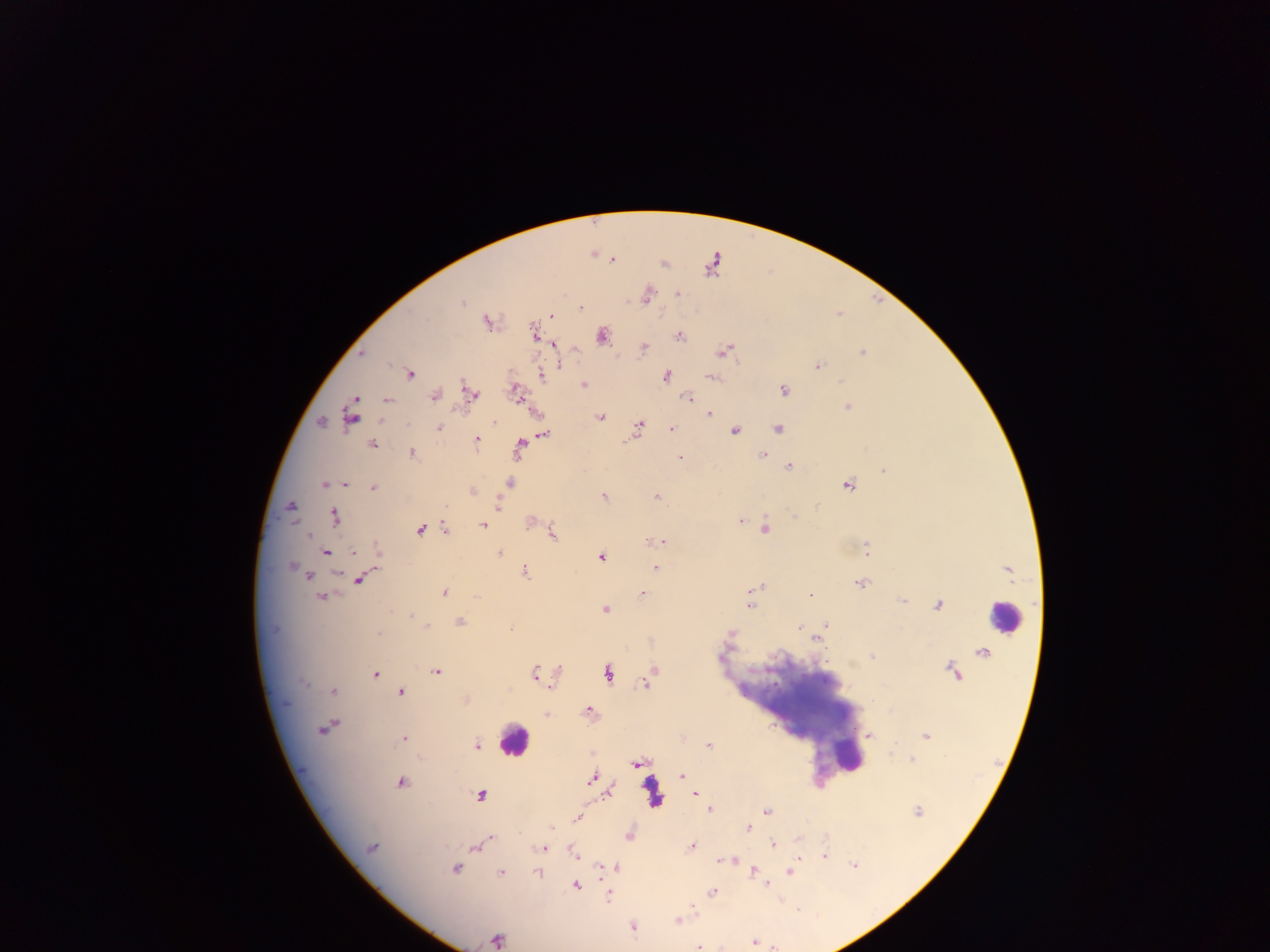

Approximate centers as {x, y} in pixels.
Summary:
  - Leukocyte locations: {1002, 618}, {512, 741}, {846, 752}
  - Malaria parasite locations: {612, 260}, {678, 293}, {646, 296}, {461, 302}, {581, 308}, {551, 316}, {426, 319}, {487, 322}, {533, 333}, {601, 336}, {679, 336}, {553, 344}, {644, 347}, {723, 351}, {862, 352}, {362, 354}, {559, 365}, {817, 366}, {410, 374}, {542, 376}, {665, 376}, {711, 377}, {583, 384}, {466, 387}, {783, 389}, {516, 392}, {469, 393}, {434, 396}, {355, 398}, {688, 398}, {387, 400}, {847, 407}, {709, 413}, {351, 417}, {601, 417}, {321, 422}, {381, 422}, {495, 422}, {639, 425}, {439, 428}, {672, 429}, {777, 429}, {736, 431}, {544, 435}, {477, 439}, {371, 444}, {520, 444}, {412, 453}, {763, 455}, {680, 458}, {789, 466}, {884, 470}, {509, 483}, {324, 484}, {346, 484}, {847, 485}, {373, 489}, {472, 491}, {656, 496}, {603, 497}, {446, 506}, {498, 506}, {290, 507}, {795, 516}, {334, 517}, {530, 522}, {740, 522}, {483, 525}, {765, 528}, {445, 529}, {419, 530}, {553, 534}, {308, 536}, {663, 542}, {867, 549}, {326, 553}, {354, 553}, {499, 553}, {378, 554}, {601, 557}, {291, 566}, {654, 569}, {525, 571}, {307, 576}, {360, 579}, {860, 583}, {756, 587}, {444, 593}, {642, 593}, {321, 596}, {477, 596}, {810, 596}, {902, 601}, {937, 605}, {750, 606}, {605, 609}, {410, 615}, {459, 622}, {826, 624}, {426, 626}, {799, 628}, {510, 629}, {731, 633}, {379, 634}, {817, 638}, {872, 656}, {559, 670}, {437, 673}, {651, 673}, {534, 674}, {608, 674}, {375, 675}, {645, 682}, {304, 683}, {552, 687}, {334, 691}, {401, 692}, {465, 700}, {588, 711}, {547, 715}, {330, 725}, {323, 728}, {869, 735}, {925, 736}, {403, 739}, {709, 746}, {477, 747}, {912, 759}, {636, 764}, {682, 775}, {590, 779}, {401, 782}, {610, 792}, {695, 794}, {480, 796}, {711, 809}, {767, 811}, {917, 811}, {579, 817}, {552, 827}, {748, 828}, {629, 835}, {490, 838}, {798, 840}, {486, 841}, {772, 844}, {693, 846}, {476, 847}, {371, 848}, {541, 848}, {574, 856}, {824, 856}, {722, 861}, {854, 865}, {616, 866}, {600, 868}, {455, 869}, {753, 871}, {500, 873}, {538, 873}, {790, 873}, {767, 884}, {577, 885}, {713, 892}, {608, 896}, {694, 907}, {677, 921}, {632, 928}, {497, 939}, {755, 942}, {699, 947}
  - Image size: 1270×952 pixels
  - Field of view: single
  - Preparation: thick blood smear
  - Country: Ghana
  - Capture: mobile-phone photograph through a microscope